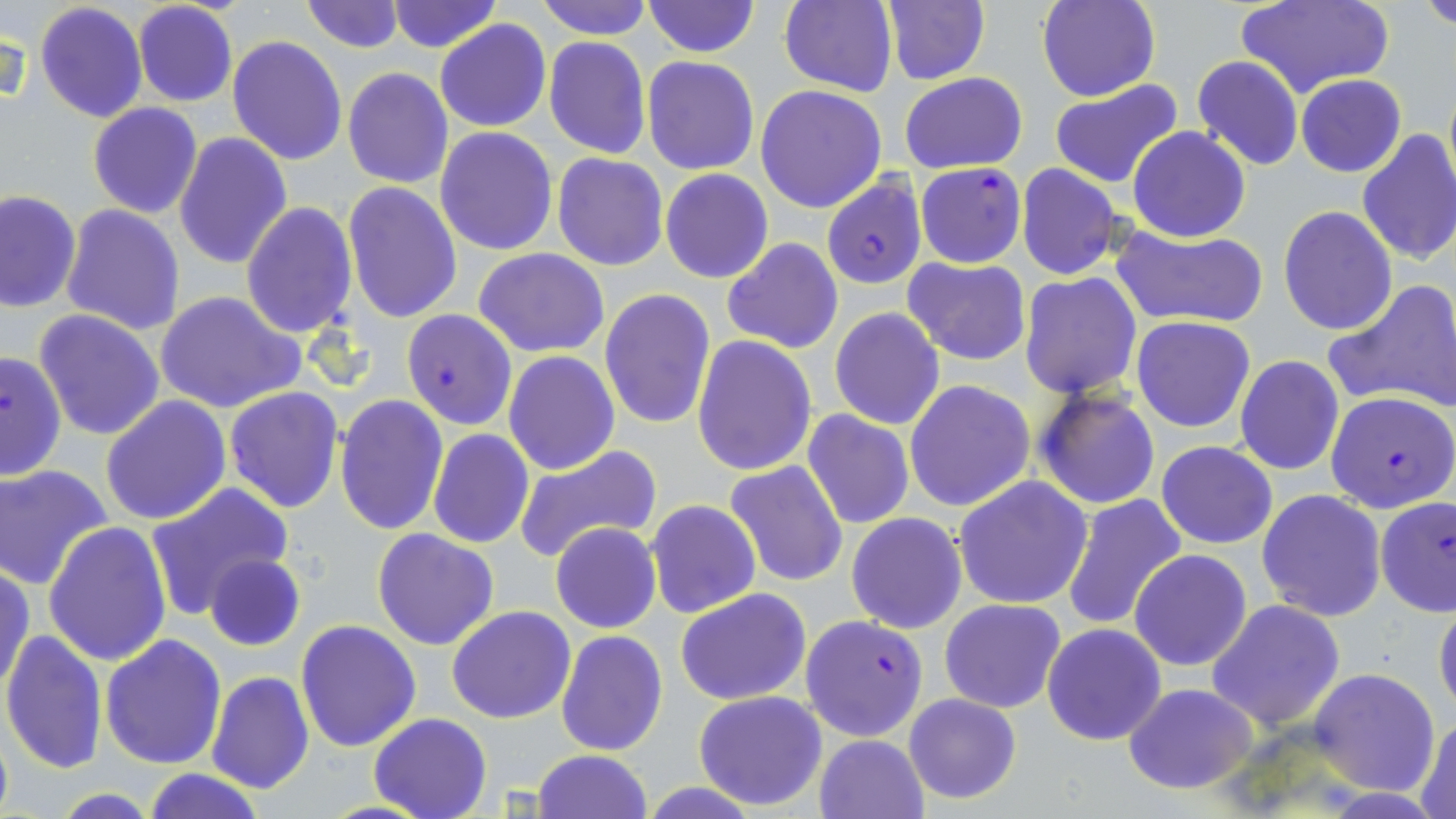

Summary:
  - Coordinate format: approximate bounding boxes as (x1, y1, x2, y2) in pixels
  - Uninfected red blood cell locations: (300, 0, 406, 52), (386, 0, 500, 53), (536, 0, 652, 40), (777, 0, 899, 96), (881, 0, 991, 86), (1038, 0, 1160, 103), (1237, 0, 1393, 101), (1421, 0, 1456, 30), (33, 1, 148, 124), (133, 1, 238, 108), (641, 1, 758, 58), (435, 19, 552, 132), (226, 35, 347, 167), (543, 36, 652, 160), (1190, 55, 1304, 171), (642, 56, 760, 174), (342, 67, 453, 189), (900, 72, 1028, 174), (1296, 74, 1405, 177), (1049, 79, 1184, 189), (756, 83, 888, 213), (88, 103, 202, 218), (435, 126, 558, 255), (1128, 126, 1251, 242), (1356, 130, 1456, 267), (173, 132, 291, 270), (553, 153, 670, 271), (1015, 163, 1124, 280), (661, 169, 773, 284), (343, 182, 464, 325), (1, 190, 82, 313), (241, 201, 358, 339), (61, 204, 186, 335), (1278, 205, 1397, 335), (1111, 224, 1269, 330), (721, 238, 844, 354), (474, 248, 610, 357), (903, 257, 1031, 366), (1019, 272, 1143, 398), (1325, 281, 1456, 416), (599, 288, 717, 430), (156, 290, 305, 414), (33, 309, 166, 443), (829, 309, 944, 430), (1132, 316, 1256, 432), (692, 335, 818, 476), (0, 348, 66, 484), (504, 350, 619, 474), (1235, 355, 1344, 475), (904, 379, 1035, 512), (224, 386, 344, 514), (1034, 387, 1161, 510), (335, 394, 449, 535), (101, 396, 231, 525), (801, 409, 915, 530), (428, 429, 535, 548), (1156, 441, 1277, 549), (514, 444, 661, 563), (725, 461, 848, 587), (0, 465, 112, 589), (674, 468, 826, 630), (954, 475, 1094, 610), (146, 482, 293, 621), (1256, 489, 1386, 621), (1059, 495, 1188, 634), (646, 499, 761, 619), (847, 513, 967, 634), (550, 522, 661, 634), (42, 523, 172, 666), (371, 527, 500, 651), (1130, 549, 1253, 671), (205, 554, 306, 651), (1, 563, 35, 698), (676, 587, 812, 706), (1433, 595, 1456, 718), (940, 597, 1068, 713), (1206, 600, 1346, 732), (447, 606, 576, 724), (477, 616, 659, 737), (296, 621, 422, 752), (1041, 623, 1166, 746), (1, 628, 107, 775), (555, 630, 668, 755), (100, 634, 227, 769), (1309, 669, 1440, 795), (206, 671, 314, 792), (1122, 683, 1259, 794), (693, 691, 828, 810), (902, 692, 1022, 804), (369, 712, 492, 819), (1414, 714, 1456, 819), (0, 718, 13, 819), (814, 734, 928, 818), (533, 750, 653, 819), (141, 766, 266, 819)
  - Plasmodium falciparum-infected red blood cell locations: (914, 162, 1026, 268), (821, 176, 927, 289), (402, 307, 518, 429), (1324, 391, 1456, 514), (1374, 496, 1455, 617), (800, 615, 928, 740)
  - Slide-level diagnosis: Plasmodium falciparum
  - Preparation: thin blood film
  - Stain: May-Grünwald-Giemsa
  - Magnification: 1000x
  - Modality: light microscopy
  - Image size: 1456×819 pixels
  - Field of view: single